State which parasite is depicted.
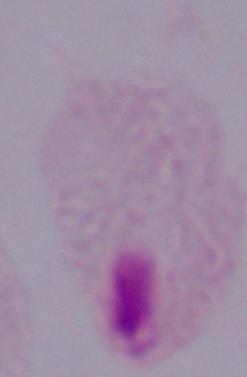

This is a trichomonad.

Captured at 1000x magnification. Photomicrograph.